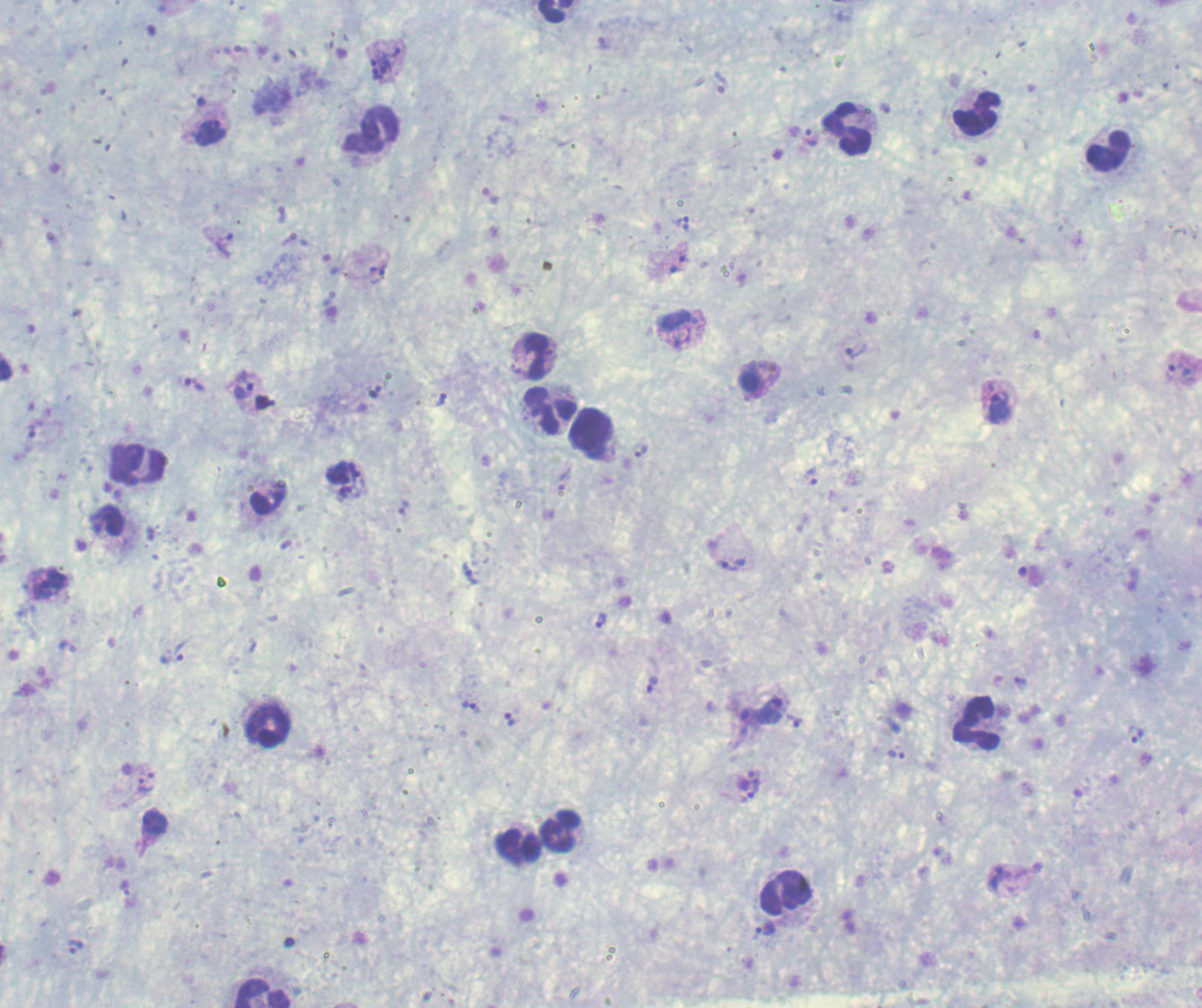

coordinate format = approximate centers as (x, y) in pixels
schizont locations = (385, 62), (344, 480)
gametocyte locations = (768, 711)
leukocyte locations = (555, 11), (977, 114), (848, 130), (371, 131), (1107, 150), (533, 355), (549, 410), (591, 435), (138, 467), (267, 498), (976, 724), (268, 725), (560, 831), (518, 846), (785, 893), (263, 994)
trophozoite locations = (602, 43), (211, 132), (810, 137), (491, 195), (281, 215), (683, 224), (225, 243), (678, 264), (376, 272), (677, 319), (856, 351), (1179, 372), (194, 384), (243, 386), (441, 400), (999, 407), (641, 451), (811, 477), (403, 507), (732, 565), (470, 573), (601, 620), (171, 659), (1020, 680), (652, 685), (471, 707), (509, 718), (795, 722), (1136, 734), (896, 754), (146, 785), (754, 789), (998, 878), (125, 888), (765, 927), (75, 946)
life-cycle stages observed = trophozoite, schizont, gametocyte
field of view = one from this slide
stain = Romanowsky
preparation = thick blood film
magnification = 100x
image size = 1202×1008 pixels
result = Plasmodium parasites detected
context = previously used in an actual diagnosis
background quality = satisfactory